Classify this cell by malaria status.
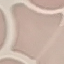
It is uninfected.

Summary:
  - Capture: smartphone camera at the microscope eyepiece
  - Image type: automatically extracted cell patch, resized to 64 × 64 pixels
  - Stain: Giemsa
  - Preparation: thin smear